Locate every blood parasite and identify its species.
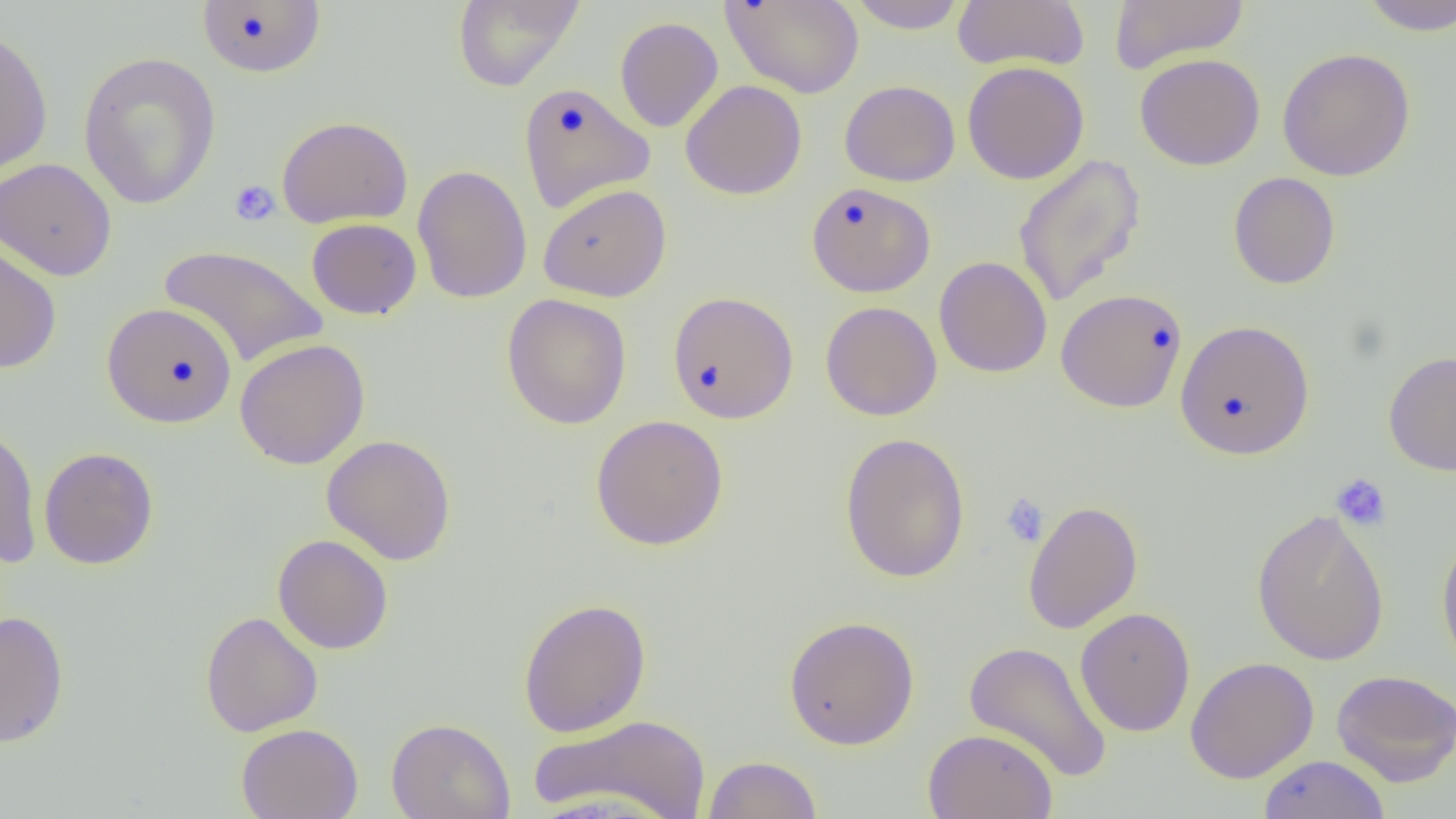
No blood parasites observed.

slide-level diagnosis = no evidence of blood parasites
modality = light microscopy
field of view = one of a larger specimen
uninfected red blood cell locations = approximate bounding boxes as [x1, y1, x2, y2] in pixels: [452, 0, 585, 91], [722, 0, 864, 98], [845, 0, 969, 34], [953, 0, 1090, 72], [1108, 0, 1249, 73], [1357, 0, 1456, 36], [197, 1, 326, 78], [614, 16, 723, 132], [0, 24, 54, 179], [1276, 47, 1416, 181], [78, 51, 221, 210], [1134, 53, 1266, 171], [962, 61, 1089, 185], [680, 79, 807, 201], [840, 79, 960, 186], [518, 82, 655, 212], [276, 116, 412, 228], [1013, 153, 1147, 309], [0, 157, 117, 282], [412, 164, 532, 304], [1228, 172, 1341, 289], [806, 182, 936, 297], [538, 184, 671, 302], [306, 218, 421, 320], [0, 238, 61, 374], [158, 244, 329, 367], [934, 256, 1052, 378], [1056, 288, 1188, 413], [667, 291, 799, 424], [502, 293, 632, 429], [820, 301, 942, 421], [102, 302, 238, 429], [1175, 319, 1314, 460], [234, 338, 370, 470], [1384, 350, 1456, 475], [590, 414, 729, 551], [0, 423, 42, 566], [839, 432, 971, 583], [321, 434, 457, 566], [39, 446, 159, 570], [1023, 500, 1143, 634], [1251, 507, 1390, 666], [1436, 533, 1456, 678], [272, 534, 393, 654], [518, 597, 652, 738], [1075, 607, 1195, 737], [1, 610, 69, 747], [200, 611, 323, 737], [783, 615, 920, 749], [963, 640, 1112, 783], [1185, 656, 1319, 783], [1331, 669, 1456, 787], [529, 714, 712, 819], [386, 717, 515, 819], [236, 723, 363, 819], [923, 728, 1058, 819], [703, 755, 822, 819], [1258, 755, 1391, 819]
preparation = thin blood smear
magnification = 1000x
image size = 1456×819 pixels
platelet locations = approximate bounding boxes as [x1, y1, x2, y2] in pixels: [228, 179, 281, 227], [1331, 473, 1391, 531], [1000, 493, 1049, 547]